Identify the cell.
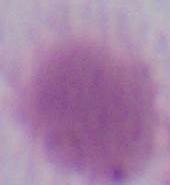

This is an erythrocyte.

magnification = 1000x
modality = micrograph